State which parasite is depicted.
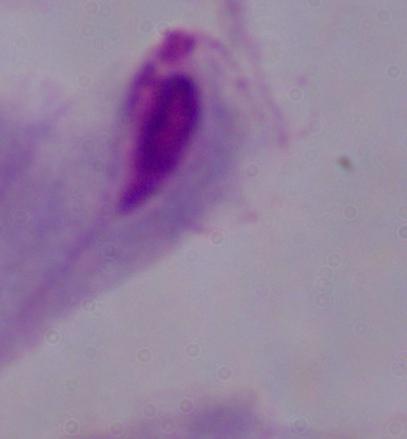

A trichomonad.

magnification: 1000x
modality: micrograph